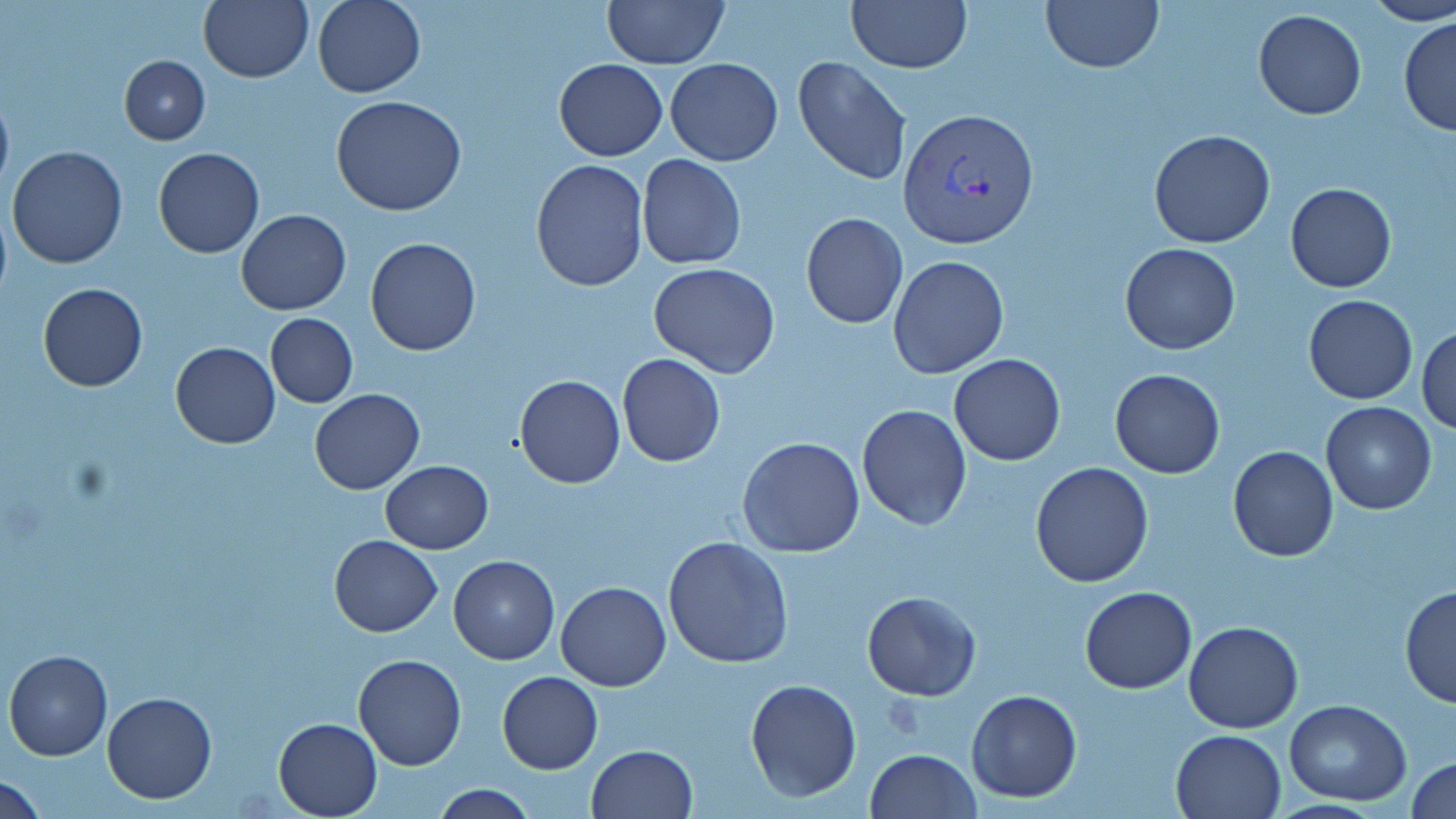

slide_level_diagnosis: Plasmodium vivax
image_size: 1456×819 pixels
field_of_view: single
plasmodium_vivax_infected_red_blood_cell_locations: 'approximate bounding boxes as (x1, y1, x2, y2) in pixels: (898, 107, 1040, 251)'
preparation: thin blood film
stain: May-Grünwald-Giemsa
magnification: 1000x
uninfected_red_blood_cell_locations: 'approximate bounding boxes as (x1, y1, x2, y2) in pixels: (199, 0, 313, 83), (313, 0, 426, 98), (602, 0, 730, 69), (846, 0, 971, 72), (1039, 0, 1165, 75), (1364, 1, 1455, 27), (1254, 8, 1367, 120), (1398, 16, 1455, 136), (119, 54, 210, 145), (793, 56, 913, 184), (554, 58, 667, 160), (664, 58, 782, 166), (0, 83, 14, 198), (330, 94, 467, 216), (1148, 129, 1276, 247), (7, 145, 128, 267), (153, 146, 264, 258), (638, 153, 746, 270), (530, 159, 649, 291), (1284, 182, 1397, 293), (236, 209, 351, 315), (799, 211, 909, 328), (365, 236, 482, 357), (1119, 244, 1240, 354), (887, 254, 1009, 378), (648, 262, 780, 379), (37, 283, 148, 391), (1303, 294, 1417, 404), (266, 313, 358, 407), (1416, 324, 1456, 435), (170, 342, 279, 448), (617, 353, 725, 466), (949, 353, 1065, 466), (1110, 369, 1224, 478), (513, 374, 625, 489), (311, 388, 425, 494), (1320, 403, 1436, 515), (857, 404, 972, 531), (737, 437, 865, 558), (1227, 446, 1338, 562), (380, 461, 493, 553), (1029, 461, 1155, 588), (329, 534, 443, 637), (663, 535, 794, 669), (448, 554, 560, 664), (556, 580, 671, 691), (1399, 584, 1456, 709), (1079, 587, 1197, 694), (862, 591, 980, 701), (1183, 620, 1304, 734), (3, 649, 113, 762), (353, 652, 466, 770), (496, 671, 602, 774), (745, 677, 862, 802), (966, 689, 1082, 803), (102, 691, 217, 804), (1282, 699, 1412, 805), (274, 717, 381, 817), (1170, 729, 1286, 819), (584, 744, 698, 819), (866, 748, 979, 819), (1407, 757, 1456, 818), (2, 776, 51, 819), (431, 785, 536, 818)'
modality: light microscopy